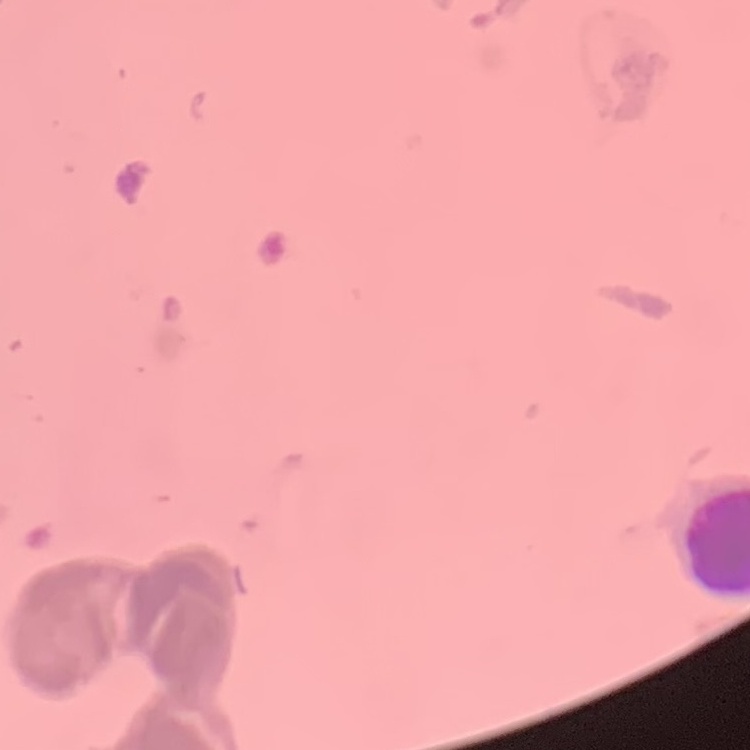

erythrocyte morphology = rouleaux formation
preparation = thin blood film
stain = Field's or Giemsa
image type = one tile cut from a larger photomicrograph